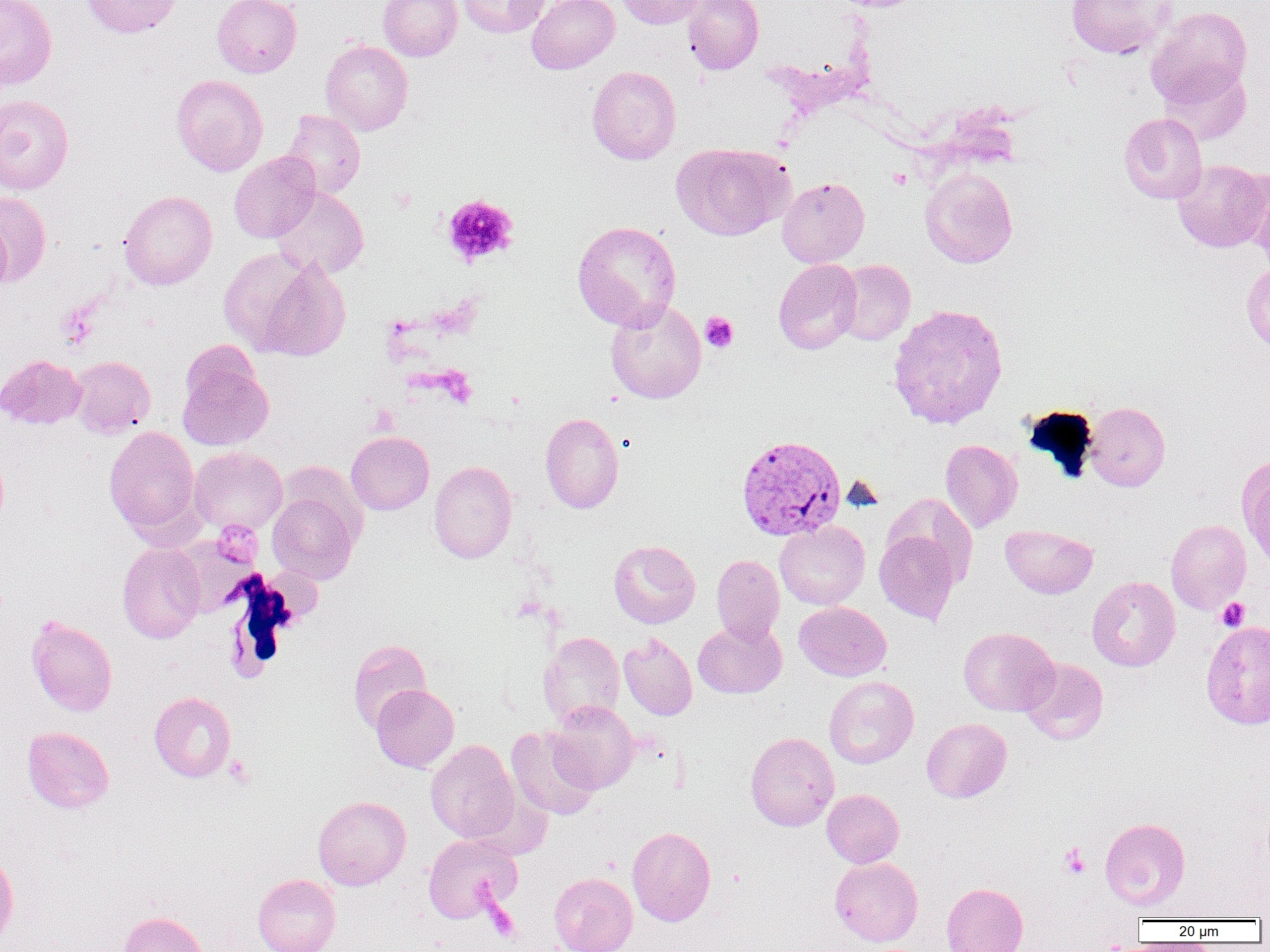
plasmodium_vivax_infected_red_blood_cell_locations: 'approximate bounding boxes as (x1, y1, x2, y2) in pixels: (736, 435, 846, 541)'
slide_level_diagnosis: Plasmodium vivax
modality: optical microscopy
preparation: thin blood smear
image_size: 1270×952 pixels
platelet_locations: 'approximate bounding boxes as (x1, y1, x2, y2) in pixels: (887, 168, 910, 189), (441, 194, 518, 267), (700, 312, 738, 352), (212, 520, 264, 569), (1217, 597, 1250, 631), (224, 755, 255, 788), (1058, 844, 1090, 879), (485, 901, 520, 941)'
field_of_view: single
magnification: 1000x
uninfected_red_blood_cell_locations: 'approximate bounding boxes as (x1, y1, x2, y2) in pixels: (0, 0, 57, 91), (81, 0, 181, 38), (212, 0, 302, 77), (378, 0, 462, 61), (458, 0, 550, 38), (527, 0, 619, 74), (616, 0, 705, 29), (682, 0, 764, 75), (1066, 0, 1173, 59), (1147, 6, 1252, 108), (321, 40, 413, 136), (1160, 64, 1252, 145), (587, 66, 681, 165), (171, 74, 268, 176), (0, 95, 73, 194), (281, 109, 365, 199), (1119, 112, 1207, 204), (670, 142, 793, 240), (228, 152, 320, 243), (1172, 159, 1269, 252), (920, 168, 1018, 268), (1241, 169, 1270, 264), (777, 177, 870, 267), (271, 187, 369, 279), (118, 190, 217, 290), (0, 191, 51, 286), (0, 218, 12, 298), (572, 220, 681, 330), (225, 249, 351, 360), (774, 259, 862, 354), (834, 260, 916, 345), (1241, 261, 1270, 353), (605, 299, 706, 403), (887, 303, 1009, 430), (0, 355, 86, 430), (70, 355, 155, 438), (177, 360, 273, 451), (1084, 402, 1170, 491), (540, 412, 624, 513), (104, 425, 201, 539), (346, 431, 434, 514), (939, 439, 1023, 532), (189, 447, 288, 535), (0, 450, 9, 530), (1237, 455, 1270, 569), (429, 460, 517, 563), (268, 492, 359, 584), (883, 494, 978, 588), (1166, 519, 1252, 613), (774, 521, 870, 609), (1000, 524, 1098, 599), (874, 529, 961, 625), (608, 540, 700, 628), (117, 543, 206, 643), (711, 554, 785, 644), (1087, 576, 1181, 671), (795, 602, 891, 681), (26, 615, 118, 717), (693, 620, 787, 699), (1201, 620, 1270, 730), (958, 627, 1059, 716), (538, 632, 625, 727), (619, 633, 697, 720), (347, 639, 431, 733), (1019, 658, 1109, 745), (824, 676, 918, 769), (371, 684, 459, 772), (149, 691, 236, 782), (546, 701, 638, 794), (922, 718, 1012, 803), (506, 725, 601, 821), (22, 726, 114, 814), (745, 732, 839, 831), (425, 740, 520, 843), (822, 789, 903, 868), (313, 795, 411, 890), (1100, 817, 1190, 911), (627, 826, 716, 926), (423, 834, 522, 922), (0, 849, 18, 946), (829, 857, 923, 946), (549, 872, 637, 952), (252, 874, 340, 952), (941, 882, 1028, 952), (119, 911, 208, 952)'